Assess the morphology of the erythrocytes.
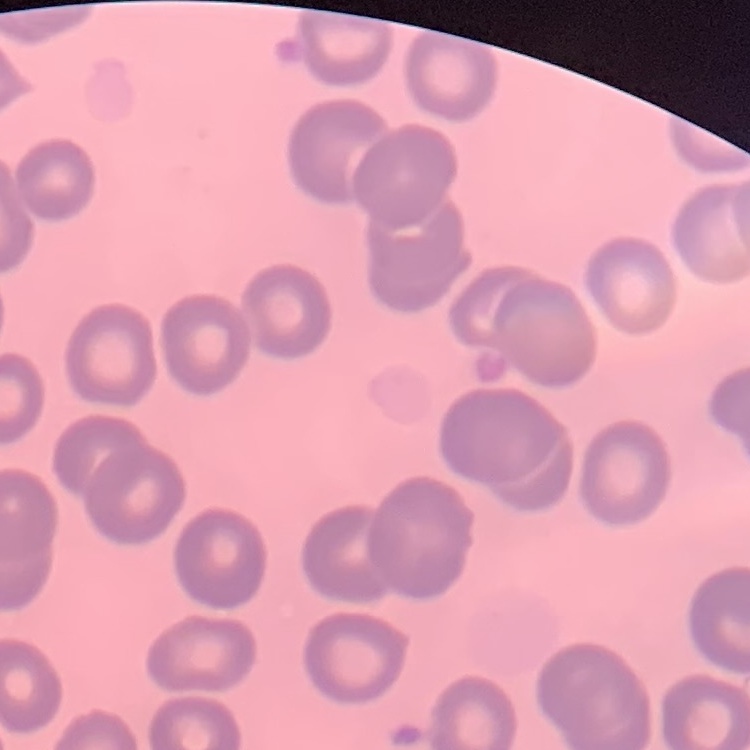

No rouleaux formation.

Field's or Giemsa stain. Thin blood smear. Square crop of a larger photomicrograph.